Locate every blood parasite and identify its species.
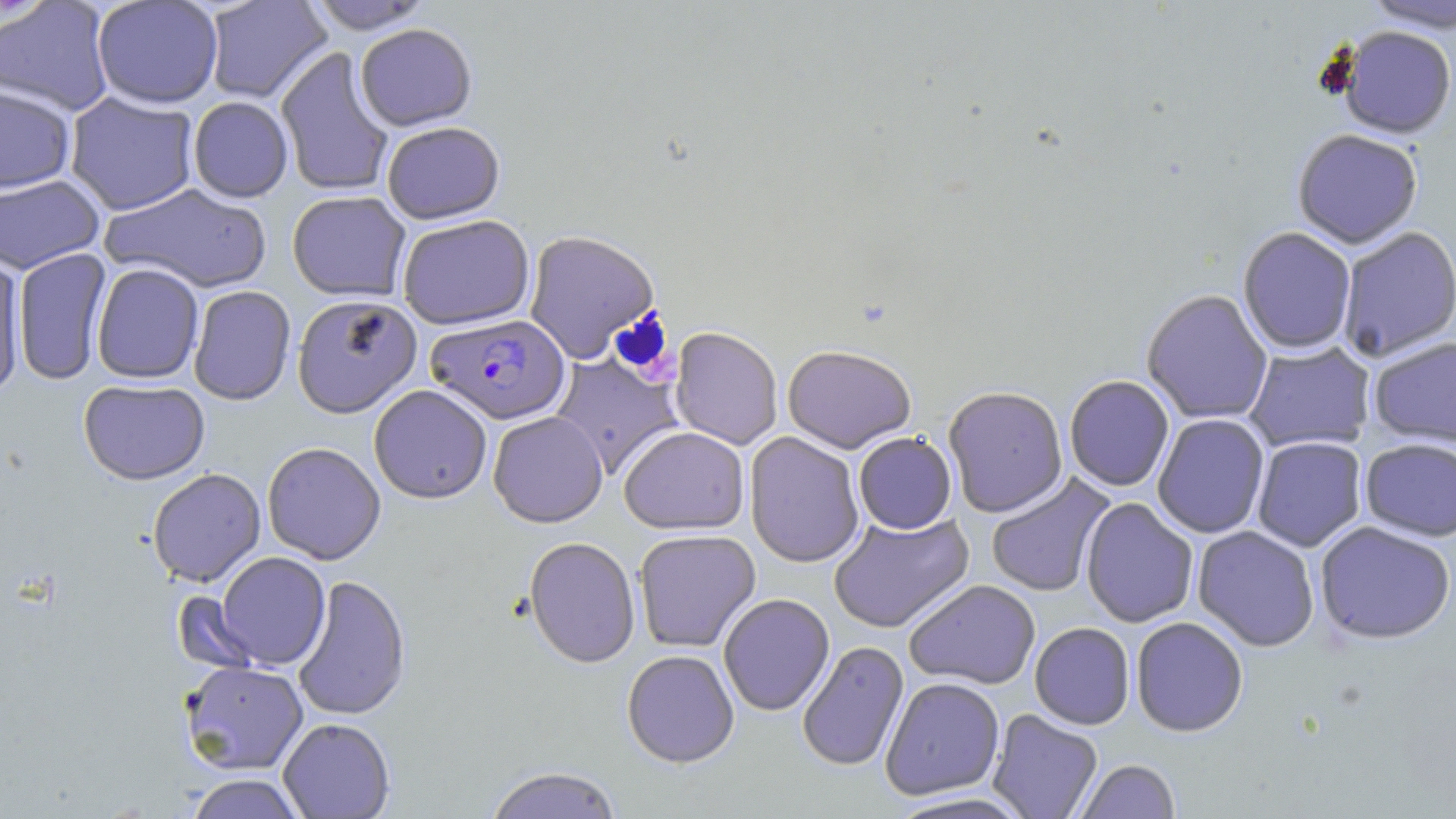

Approximate bounding boxes as named x1/y1/x2/y2 corners in pixels.
Plasmodium falciparum-infected red blood cells: (x1=426, y1=314, x2=571, y2=425).
No Plasmodium ovale, Plasmodium malariae, Plasmodium vivax, Babesia divergens, or Trypanosoma brucei observed.

Uninfected red blood cell locations: (x1=91, y1=0, x2=224, y2=109), (x1=203, y1=0, x2=332, y2=104), (x1=1362, y1=0, x2=1456, y2=33), (x1=0, y1=1, x2=116, y2=116), (x1=305, y1=1, x2=434, y2=34), (x1=354, y1=23, x2=477, y2=131), (x1=1337, y1=26, x2=1455, y2=140), (x1=275, y1=46, x2=394, y2=197), (x1=0, y1=84, x2=76, y2=194), (x1=64, y1=92, x2=200, y2=215), (x1=187, y1=96, x2=293, y2=203), (x1=381, y1=121, x2=505, y2=224), (x1=1292, y1=129, x2=1423, y2=249), (x1=0, y1=174, x2=104, y2=274), (x1=102, y1=183, x2=272, y2=294), (x1=287, y1=190, x2=411, y2=301), (x1=396, y1=214, x2=535, y2=330), (x1=1238, y1=227, x2=1357, y2=354), (x1=1337, y1=227, x2=1456, y2=362), (x1=523, y1=229, x2=660, y2=364), (x1=13, y1=248, x2=112, y2=386), (x1=0, y1=256, x2=26, y2=400), (x1=91, y1=263, x2=204, y2=384), (x1=188, y1=285, x2=296, y2=405), (x1=1141, y1=289, x2=1273, y2=425), (x1=292, y1=294, x2=422, y2=417), (x1=669, y1=327, x2=783, y2=450), (x1=1368, y1=336, x2=1456, y2=447), (x1=1244, y1=342, x2=1375, y2=452), (x1=783, y1=344, x2=917, y2=453), (x1=549, y1=353, x2=683, y2=480), (x1=1064, y1=374, x2=1174, y2=492), (x1=78, y1=379, x2=210, y2=485), (x1=368, y1=384, x2=493, y2=504), (x1=943, y1=385, x2=1069, y2=517), (x1=488, y1=411, x2=608, y2=527), (x1=1152, y1=413, x2=1270, y2=539), (x1=619, y1=426, x2=749, y2=534), (x1=745, y1=432, x2=865, y2=568), (x1=853, y1=432, x2=957, y2=534), (x1=1251, y1=436, x2=1367, y2=552), (x1=1359, y1=438, x2=1456, y2=541), (x1=262, y1=441, x2=386, y2=565), (x1=147, y1=468, x2=266, y2=587), (x1=985, y1=472, x2=1116, y2=598), (x1=1080, y1=497, x2=1199, y2=628), (x1=828, y1=511, x2=974, y2=633), (x1=1314, y1=521, x2=1456, y2=645), (x1=1192, y1=526, x2=1320, y2=652), (x1=633, y1=529, x2=761, y2=652), (x1=523, y1=536, x2=640, y2=668), (x1=215, y1=552, x2=330, y2=670), (x1=291, y1=574, x2=411, y2=721), (x1=904, y1=579, x2=1041, y2=689), (x1=170, y1=590, x2=264, y2=675), (x1=718, y1=593, x2=835, y2=716), (x1=1131, y1=616, x2=1248, y2=737), (x1=1030, y1=622, x2=1134, y2=730), (x1=796, y1=640, x2=909, y2=773), (x1=622, y1=649, x2=739, y2=767), (x1=180, y1=661, x2=309, y2=775), (x1=880, y1=677, x2=1005, y2=801), (x1=987, y1=709, x2=1103, y2=819), (x1=278, y1=717, x2=395, y2=818), (x1=1075, y1=759, x2=1181, y2=819), (x1=483, y1=765, x2=624, y2=819), (x1=182, y1=773, x2=309, y2=818), (x1=884, y1=792, x2=1040, y2=818). Slide-level diagnosis: Plasmodium falciparum. One field of a larger specimen. Thin blood smear. May-Grünwald-Giemsa-stained preparation. Captured at 1000x magnification. Image is 1456×819 pixels. Optical microscopy.